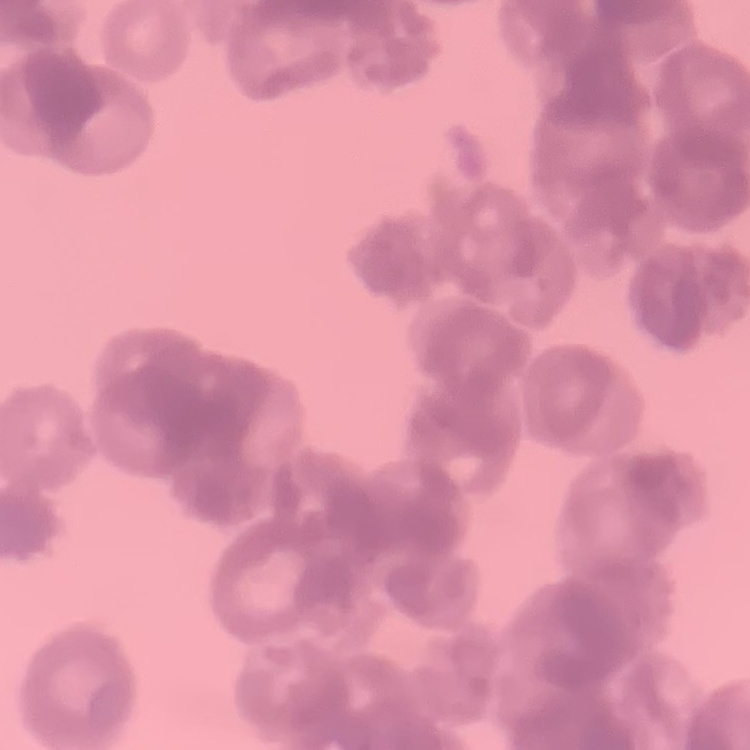 The erythrocytes show rouleaux formation. Stained with either Field's or Giemsa. Thin blood smear. One tile cut from a larger photomicrograph.